Locate every leukocyte (white blood cell).
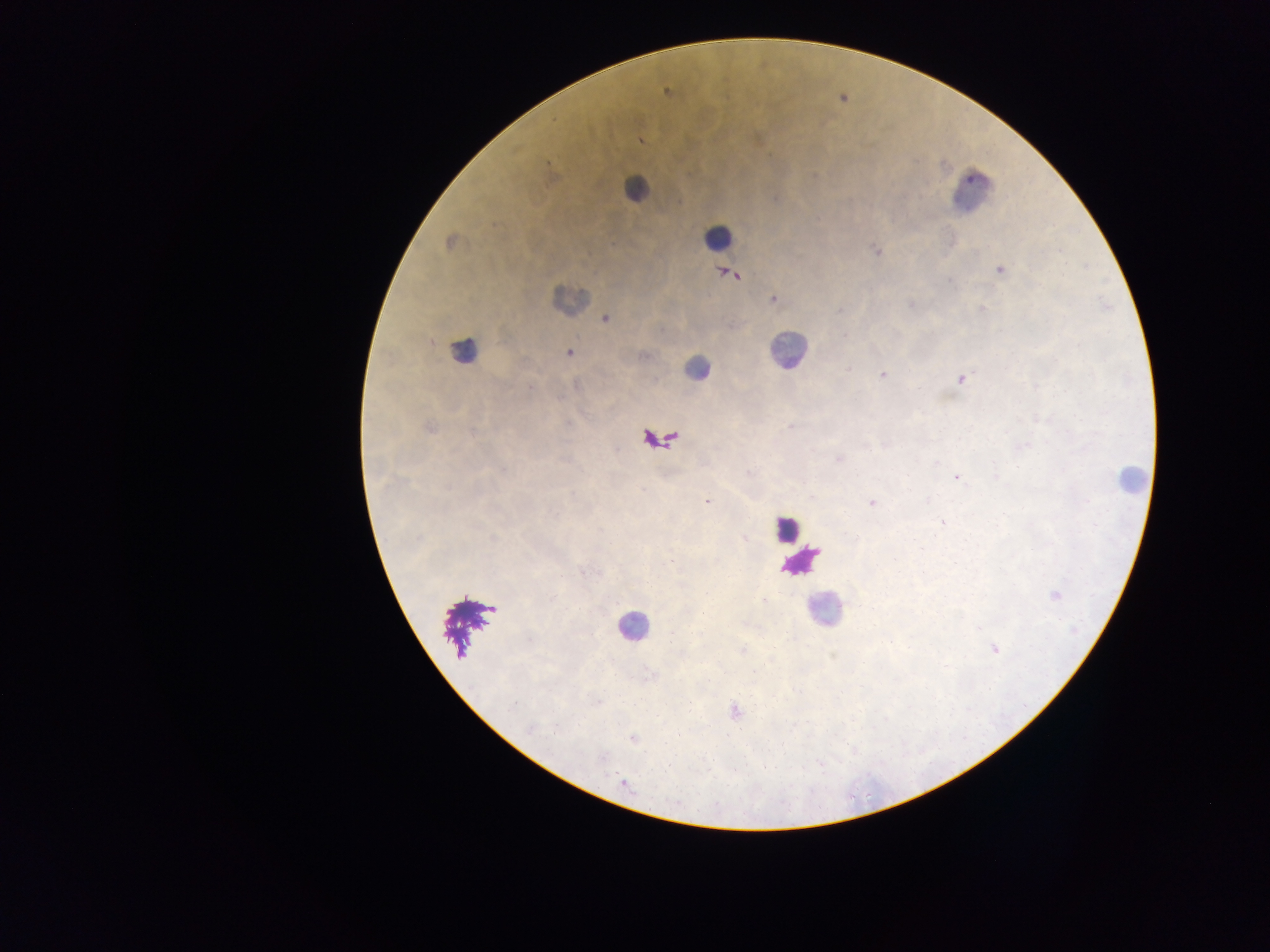

Approximate centers as [x, y] in pixels.
Leukocytes: [639, 186], [974, 195], [714, 237], [464, 352], [791, 353], [692, 373], [1125, 481], [821, 613], [632, 627].

Summary:
  - Plasmodium parasite locations: [640, 140], [814, 174], [446, 242], [876, 251], [998, 268], [723, 271], [735, 276], [948, 281], [774, 298], [910, 305], [981, 307], [838, 312], [604, 318], [1076, 344], [568, 353], [847, 369], [882, 374], [959, 378], [530, 387], [788, 426], [838, 458], [749, 472], [956, 478], [448, 489], [643, 492], [707, 502], [869, 502], [942, 522], [744, 538], [582, 572], [1055, 595], [764, 601], [528, 642], [994, 648], [741, 649], [597, 702], [529, 729], [633, 739], [622, 783]
  - Image size: 1270×952 pixels
  - Preparation: thick blood smear
  - Capture: mobile-phone photograph through a microscope
  - Field of view: single
  - Country: Ghana